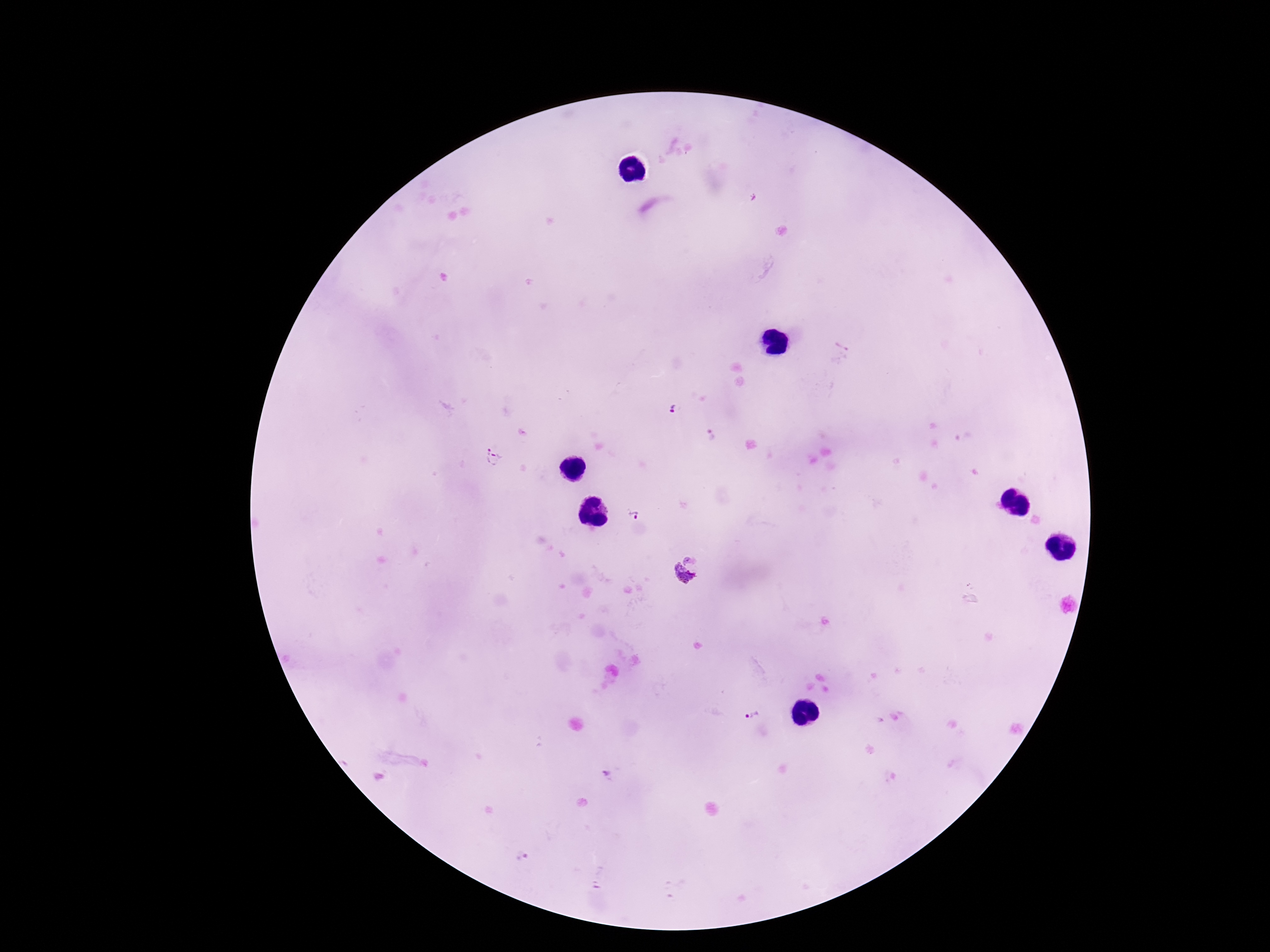
Approximate object centers, in pixels from the top-left corner.
Summary:
  - Plasmodium parasite locations: (x=673, y=410), (x=712, y=434), (x=495, y=456), (x=633, y=515), (x=690, y=559), (x=679, y=580), (x=751, y=716), (x=607, y=777), (x=521, y=855)
  - Field of view: single
  - Magnification: 100x
  - Image size: 1270×952 pixels
  - Capture: smartphone camera through the microscope eyepiece
  - Patient malaria status: positive
  - Preparation: thick blood film
  - Stain: Giemsa